Assess this cell for malaria.
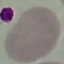

Uninfected.

Giemsa stain. Automatically extracted cell patch, resized to 64 × 64 pixels. Photographed with a smartphone camera at the microscope eyepiece. Thin blood smear.